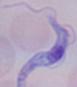

A trypanosome is seen. Micrograph. 1000x magnification.